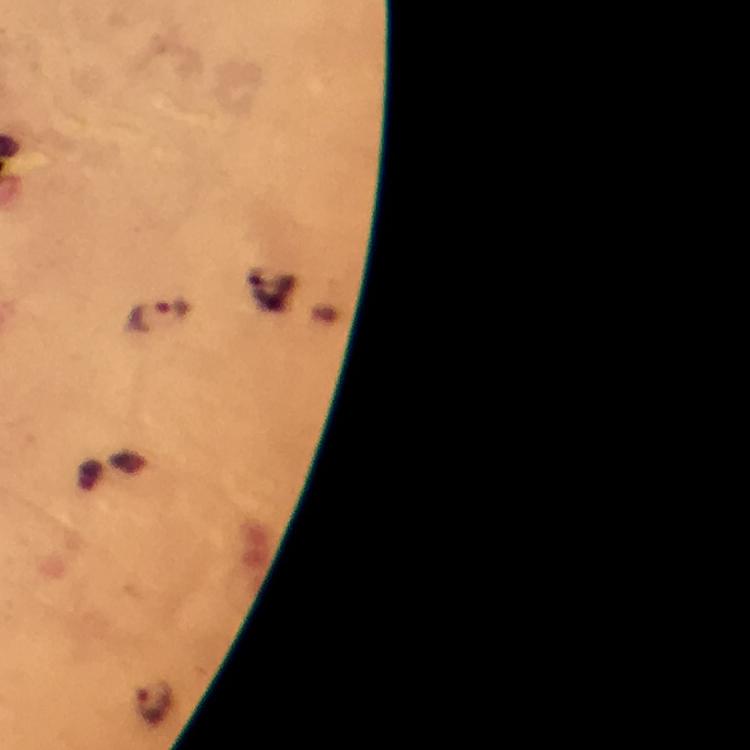
capture: smartphone camera through the microscope
image_size: 750×750 pixels
malaria_parasite_locations: 'approximate centers as (x, y) in pixels: (160, 314), (154, 704)'
preparation: thick blood film
cropped_from: a single field of view
context: from a diagnostic examination for malaria
stain: Giemsa
immersion_oil: used
magnification: 100x